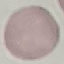
malaria status = uninfected
preparation = thin smear
image type = cell patch, automatically extracted from a larger field of view and resized to 64 × 64 pixels
capture = smartphone camera at the microscope eyepiece
stain = Giemsa